Identify the parasite.
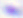

This is Toxoplasma gondii.

Captured at 400x magnification. Micrograph.